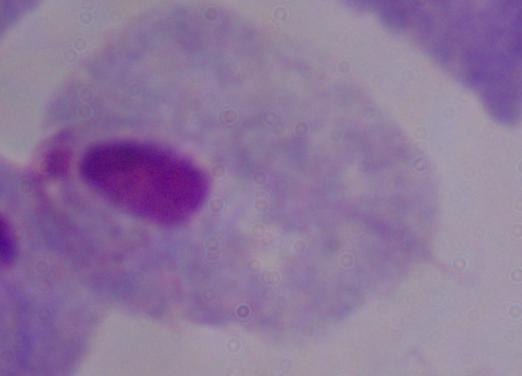
Summary:
  - Identification: trichomonad
  - Magnification: 1000x
  - Modality: photomicrograph